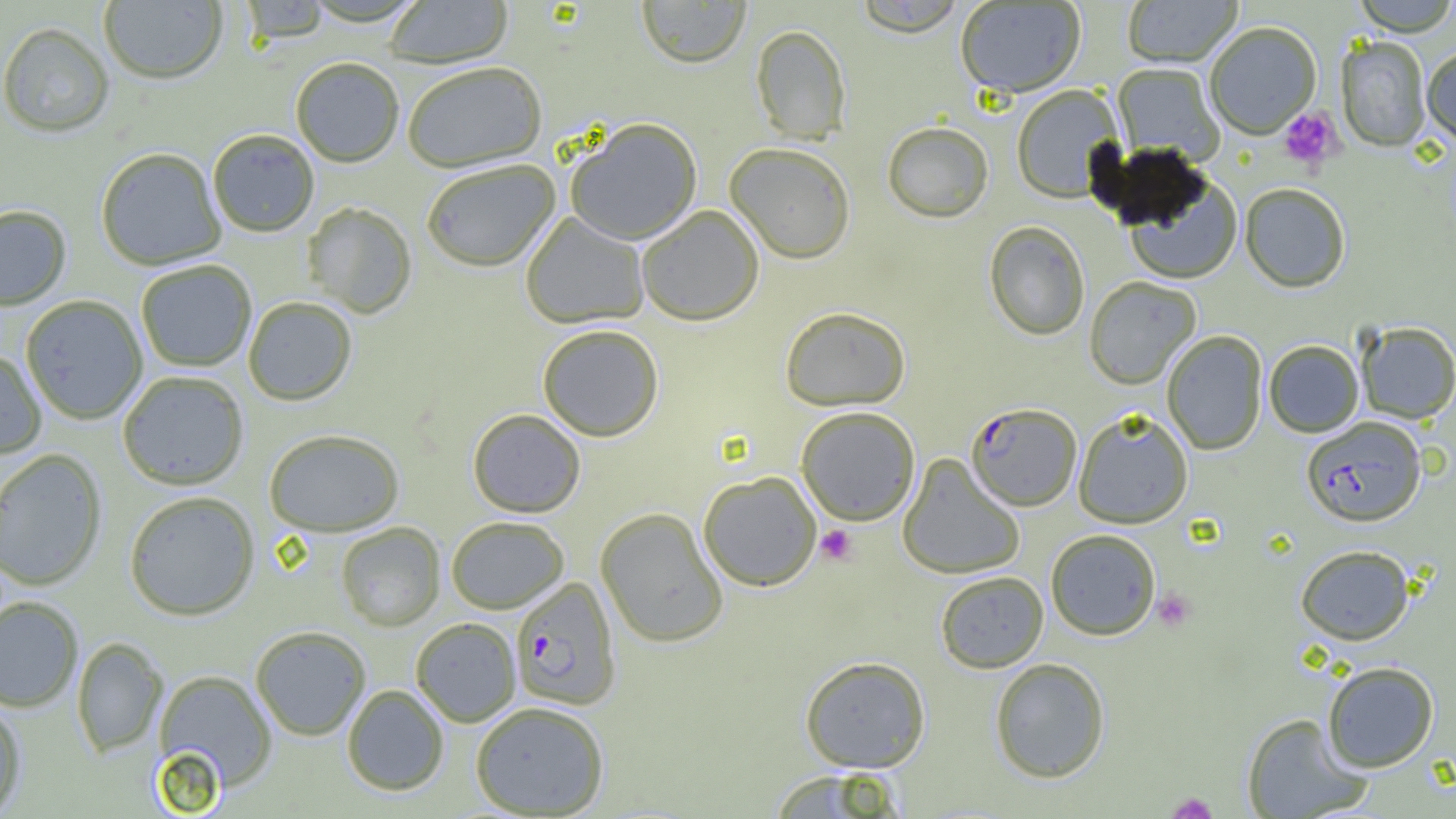
Plasmodium falciparum-infected red blood cell locations = approximate bounding boxes as named x1/y1/x2/y2 corners in pixels: (x1=966, y1=402, x2=1081, y2=511), (x1=1301, y1=416, x2=1426, y2=527), (x1=509, y1=577, x2=621, y2=711)
slide-level diagnosis = Plasmodium falciparum
image size = 1456×819 pixels
modality = light microscopy
preparation = thin blood film
platelet locations = approximate bounding boxes as named x1/y1/x2/y2 corners in pixels: (x1=1278, y1=108, x2=1342, y2=170), (x1=815, y1=526, x2=858, y2=566), (x1=1152, y1=588, x2=1196, y2=632), (x1=1166, y1=793, x2=1218, y2=818)
magnification = 1000x
field of view = single
uninfected red blood cell locations = approximate bounding boxes as named x1/y1/x2/y2 corners in pixels: (x1=100, y1=0, x2=227, y2=86), (x1=383, y1=0, x2=513, y2=71), (x1=636, y1=0, x2=751, y2=70), (x1=852, y1=0, x2=967, y2=38), (x1=1121, y1=0, x2=1242, y2=67), (x1=1351, y1=0, x2=1456, y2=37), (x1=238, y1=1, x2=331, y2=47), (x1=955, y1=1, x2=1086, y2=98), (x1=1204, y1=22, x2=1322, y2=139), (x1=0, y1=24, x2=114, y2=140), (x1=751, y1=26, x2=851, y2=145), (x1=1335, y1=36, x2=1431, y2=153), (x1=1422, y1=47, x2=1456, y2=148), (x1=291, y1=60, x2=404, y2=168), (x1=1112, y1=63, x2=1224, y2=164), (x1=403, y1=65, x2=548, y2=175), (x1=1011, y1=85, x2=1124, y2=203), (x1=565, y1=120, x2=703, y2=246), (x1=882, y1=122, x2=993, y2=223), (x1=208, y1=131, x2=319, y2=238), (x1=725, y1=145, x2=855, y2=265), (x1=96, y1=149, x2=226, y2=271), (x1=422, y1=162, x2=561, y2=274), (x1=1124, y1=174, x2=1242, y2=285), (x1=1239, y1=183, x2=1351, y2=293), (x1=302, y1=203, x2=417, y2=319), (x1=0, y1=206, x2=71, y2=312), (x1=637, y1=206, x2=764, y2=327), (x1=521, y1=212, x2=649, y2=329), (x1=984, y1=221, x2=1090, y2=341), (x1=137, y1=261, x2=256, y2=372), (x1=1084, y1=276, x2=1201, y2=390), (x1=21, y1=296, x2=147, y2=425), (x1=244, y1=298, x2=357, y2=407), (x1=779, y1=306, x2=911, y2=412), (x1=1356, y1=321, x2=1456, y2=424), (x1=537, y1=326, x2=663, y2=443), (x1=1161, y1=330, x2=1267, y2=455), (x1=1263, y1=340, x2=1364, y2=437), (x1=0, y1=350, x2=47, y2=459), (x1=118, y1=372, x2=249, y2=491), (x1=796, y1=407, x2=920, y2=526), (x1=1072, y1=409, x2=1193, y2=529), (x1=467, y1=410, x2=586, y2=519), (x1=264, y1=430, x2=404, y2=538), (x1=0, y1=449, x2=108, y2=592), (x1=897, y1=454, x2=1025, y2=580), (x1=697, y1=472, x2=822, y2=592), (x1=124, y1=492, x2=260, y2=622), (x1=595, y1=508, x2=728, y2=648), (x1=446, y1=518, x2=569, y2=614), (x1=337, y1=522, x2=445, y2=632), (x1=1045, y1=529, x2=1161, y2=640), (x1=1295, y1=544, x2=1416, y2=645), (x1=935, y1=570, x2=1048, y2=673), (x1=0, y1=597, x2=83, y2=713), (x1=411, y1=618, x2=521, y2=727), (x1=251, y1=627, x2=371, y2=741), (x1=72, y1=637, x2=168, y2=758), (x1=799, y1=655, x2=931, y2=773), (x1=989, y1=657, x2=1111, y2=783), (x1=1322, y1=661, x2=1439, y2=772), (x1=152, y1=670, x2=277, y2=794), (x1=342, y1=685, x2=449, y2=796), (x1=0, y1=701, x2=26, y2=818), (x1=470, y1=702, x2=609, y2=818), (x1=1241, y1=713, x2=1370, y2=819), (x1=766, y1=769, x2=908, y2=817)